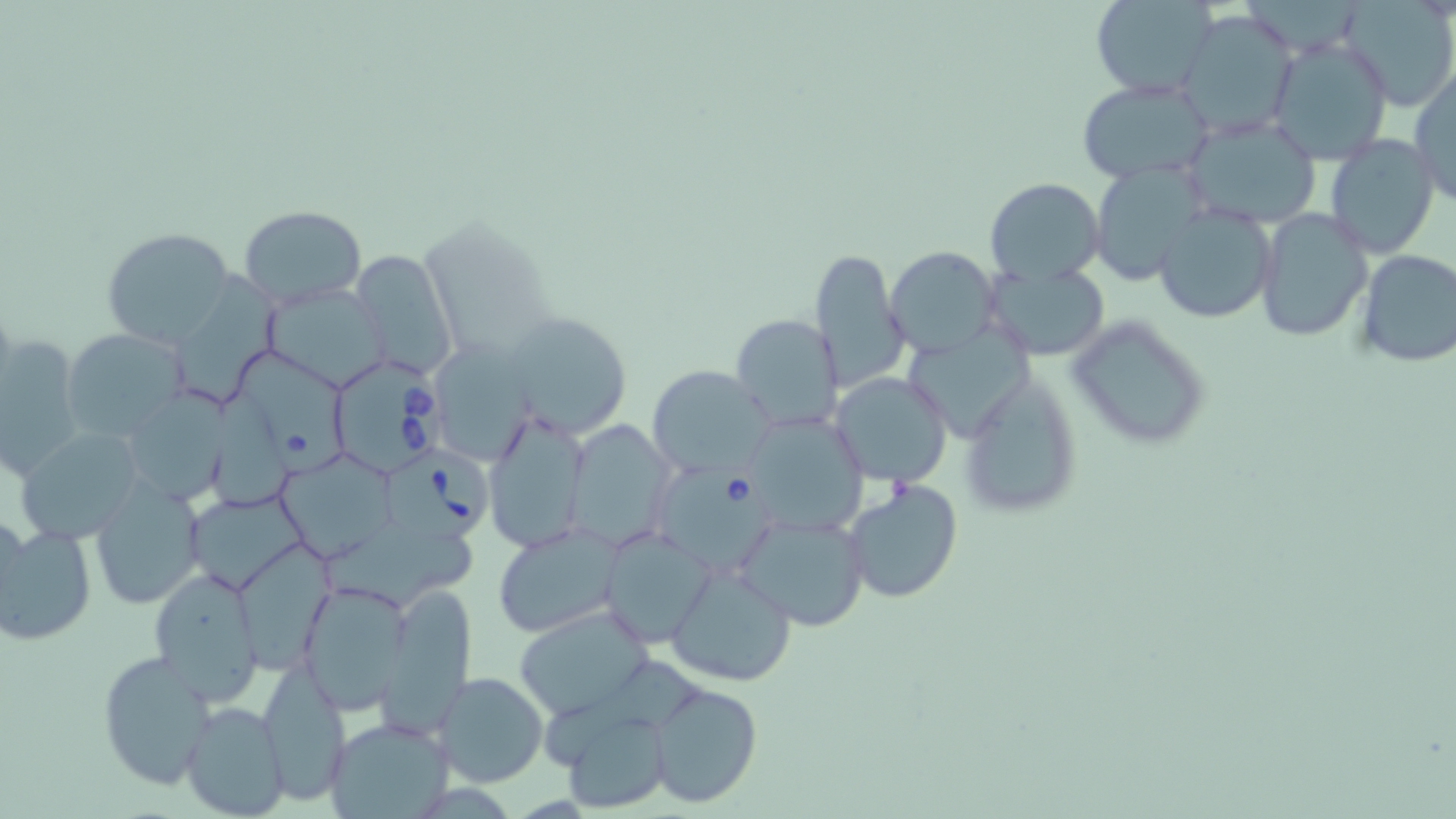
slide-level diagnosis = Babesia divergens
field of view = single
modality = light microscopy
image size = 1456×819 pixels
preparation = thin blood smear
stain = May-Grünwald-Giemsa
uninfected red blood cell locations = approximate bounding boxes as [x1, y1, x2, y2] in pixels: [1088, 0, 1218, 99], [1340, 0, 1455, 112], [1175, 8, 1301, 137], [1266, 37, 1394, 164], [1410, 67, 1455, 206], [1077, 76, 1216, 185], [1178, 112, 1325, 231], [1323, 135, 1440, 259], [1086, 159, 1209, 285], [984, 177, 1105, 287], [1154, 202, 1279, 321], [239, 204, 366, 307], [1255, 206, 1373, 341], [101, 226, 235, 346], [887, 247, 1000, 357], [351, 248, 461, 377], [807, 249, 908, 390], [1355, 249, 1456, 369], [985, 261, 1109, 361], [173, 264, 288, 400], [265, 279, 396, 395], [502, 311, 633, 440], [730, 313, 844, 432], [1064, 314, 1214, 451], [907, 325, 1041, 439], [63, 327, 187, 439], [0, 332, 84, 480], [434, 336, 545, 466], [234, 345, 350, 479], [648, 366, 774, 476], [959, 368, 1085, 520], [830, 372, 953, 487], [121, 390, 230, 508], [483, 409, 592, 555], [744, 412, 871, 534], [568, 421, 672, 550], [15, 425, 148, 544], [269, 446, 404, 555], [88, 476, 206, 609], [844, 479, 963, 604], [189, 490, 311, 593], [736, 511, 870, 632], [0, 520, 96, 646], [318, 521, 493, 611], [492, 523, 624, 639], [600, 525, 717, 647], [238, 543, 336, 668], [665, 560, 798, 686], [148, 566, 264, 707], [299, 582, 412, 713], [514, 605, 654, 718], [96, 649, 217, 792], [257, 664, 350, 805], [433, 673, 548, 788], [647, 682, 762, 807], [180, 701, 288, 819], [553, 707, 676, 814], [324, 716, 453, 818]
Babesia divergens-infected red blood cell locations = approximate bounding boxes as [x1, y1, x2, y2] in pixels: [328, 354, 448, 479], [381, 444, 496, 541], [660, 463, 777, 574]
magnification = 1000x